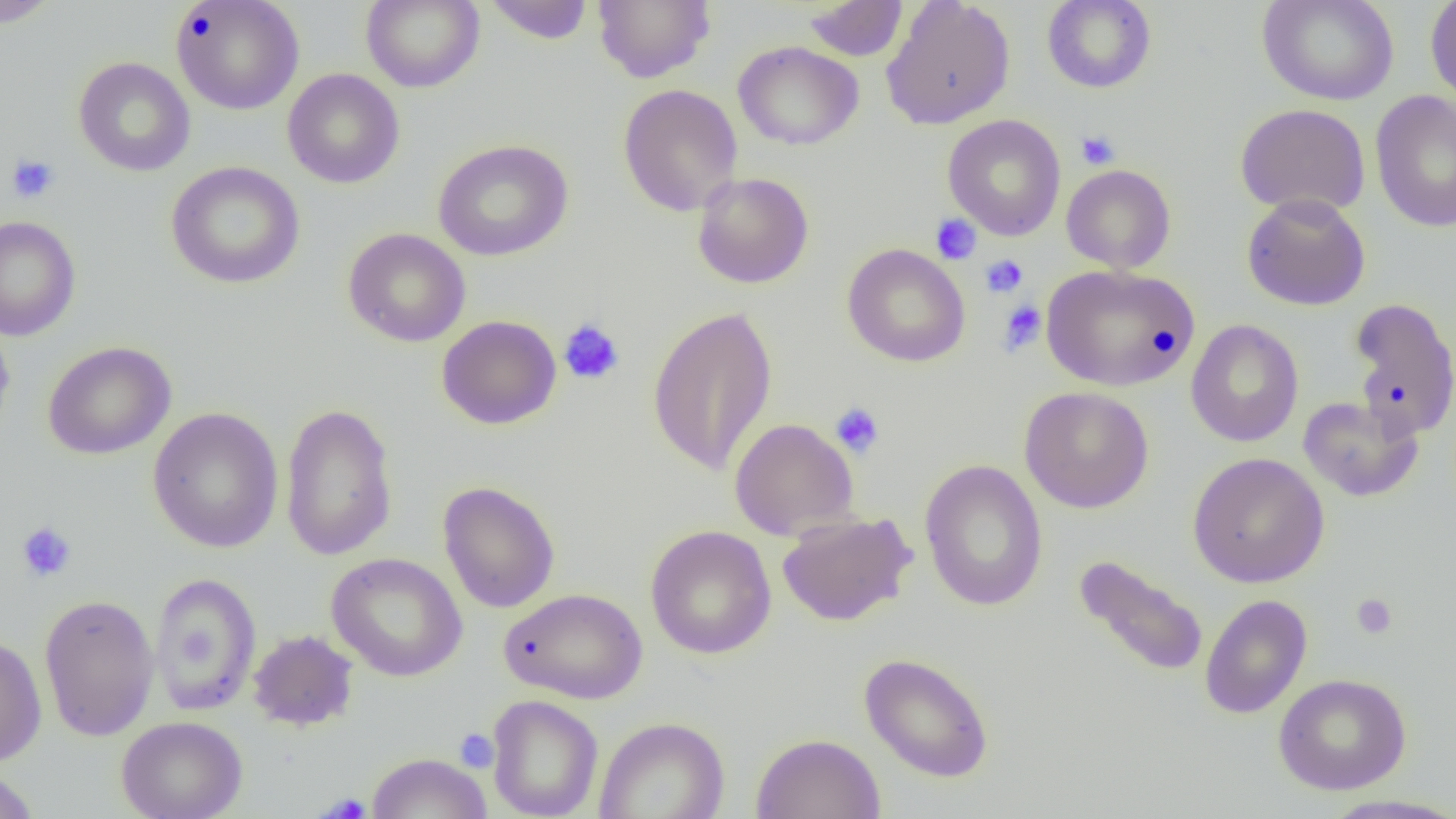
Approximate bounding boxes as [x1, y1, x2, y2] in pixels. Platelet locations: [1076, 129, 1121, 169], [6, 153, 60, 204], [930, 214, 981, 265], [980, 254, 1028, 298], [998, 300, 1047, 355], [558, 319, 625, 385], [830, 402, 885, 457], [16, 521, 77, 583], [1351, 593, 1398, 639], [454, 728, 499, 773], [319, 793, 371, 818]. Uninfected red blood cell locations: [0, 0, 62, 28], [171, 0, 304, 115], [361, 0, 485, 92], [484, 0, 595, 44], [593, 0, 715, 84], [881, 0, 1016, 130], [1042, 0, 1156, 93], [1257, 0, 1399, 105], [1425, 0, 1456, 105], [802, 1, 908, 61], [733, 41, 864, 151], [73, 57, 196, 177], [282, 69, 405, 188], [618, 84, 743, 217], [1370, 89, 1456, 233], [1234, 103, 1371, 217], [942, 114, 1066, 241], [432, 139, 573, 262], [165, 161, 305, 288], [1061, 164, 1176, 273], [692, 172, 814, 289], [1241, 193, 1371, 311], [0, 215, 81, 341], [343, 228, 471, 348], [842, 243, 971, 367], [1040, 263, 1199, 391], [1348, 297, 1456, 439], [646, 305, 778, 476], [0, 315, 15, 445], [436, 315, 561, 430], [1186, 319, 1304, 448], [42, 341, 176, 460], [1019, 386, 1154, 513], [1297, 396, 1424, 502], [280, 402, 398, 562], [147, 407, 284, 553], [729, 418, 858, 539], [1187, 451, 1329, 589], [919, 458, 1049, 612], [438, 481, 560, 613], [776, 511, 916, 627], [644, 524, 777, 659], [326, 553, 468, 682], [1073, 554, 1210, 678], [149, 571, 262, 716], [499, 588, 648, 704], [38, 593, 159, 742], [1199, 594, 1312, 719], [248, 630, 358, 731], [0, 634, 47, 766], [859, 652, 995, 783], [1273, 673, 1412, 795], [487, 694, 603, 819], [116, 716, 248, 819], [594, 716, 730, 819], [750, 733, 886, 819], [367, 752, 492, 819], [0, 768, 40, 819], [1316, 794, 1456, 819]. Slide-level diagnosis: negative for blood parasites. Captured at 1000x magnification. Single field of view. Light microscopy. Image is 1456×819 pixels. Thin blood film.